Assess this cell for malaria.
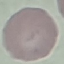

It is uninfected.

capture = smartphone camera at the microscope eyepiece
image type = automatically extracted cell patch, resized to 64 × 64 pixels
preparation = thin smear
stain = Giemsa